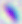
{
  "identification": "Toxoplasma gondii",
  "modality": "photomicrograph",
  "magnification": "400x"
}